Classify this cell by malaria status.
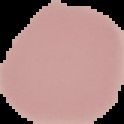

It is uninfected.

Segmented cell region on a black background. From a thin blood film. Image is 124×124 pixels.